Comment on the morphology of the red blood cells.
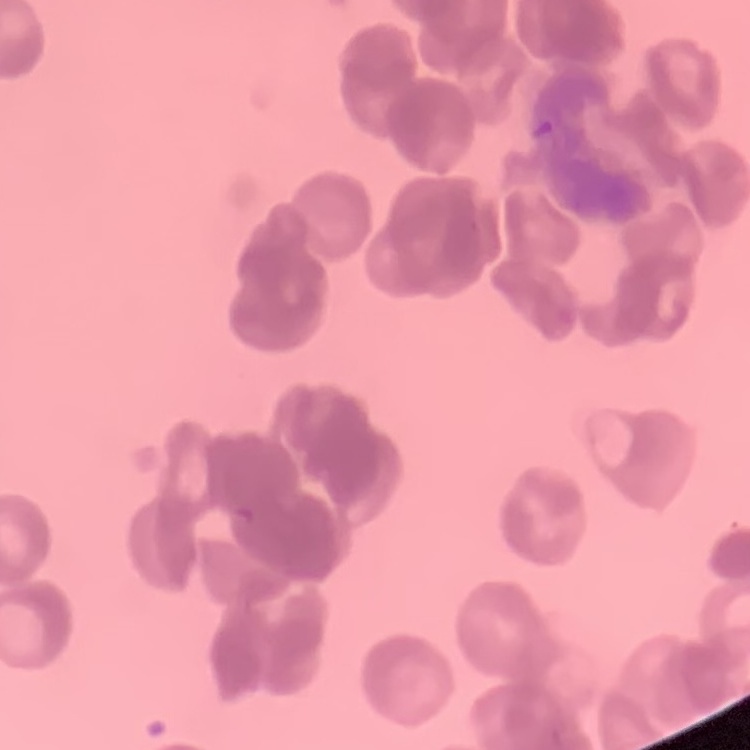
They show rouleaux formation.

Summary:
  - Image type: square crop of a larger photomicrograph
  - Stain: Field's or Giemsa
  - Preparation: thin blood smear